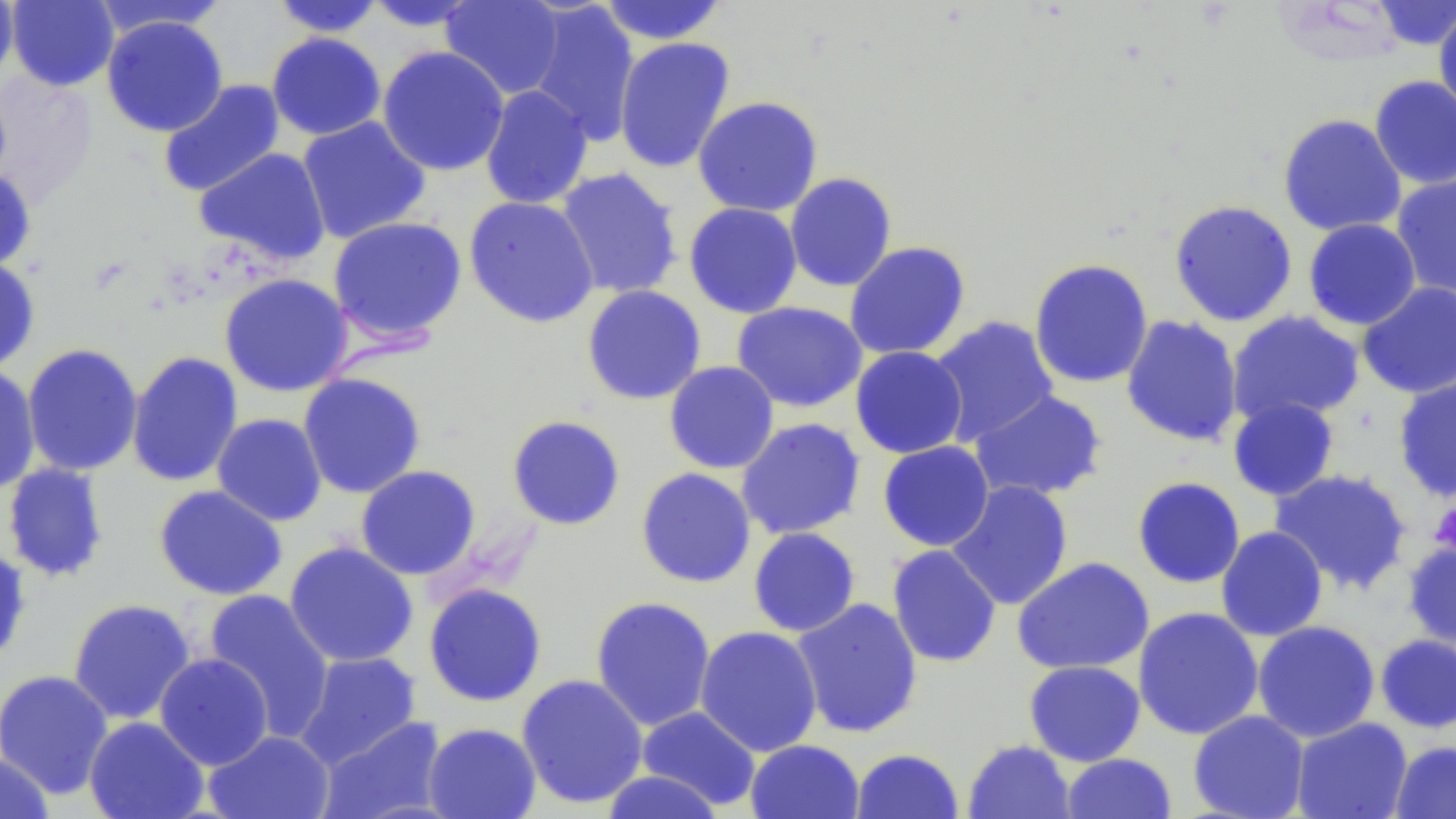
Summary:
  - Coordinate format: approximate bounding boxes as named x1/y1/x2/y2 corners in pixels
  - Platelet locations: (x1=1428, y1=501, x2=1456, y2=556)
  - Uninfected red blood cell locations: (x1=0, y1=0, x2=18, y2=87), (x1=6, y1=0, x2=120, y2=91), (x1=270, y1=0, x2=386, y2=37), (x1=440, y1=0, x2=566, y2=100), (x1=597, y1=0, x2=728, y2=45), (x1=361, y1=1, x2=485, y2=32), (x1=525, y1=1, x2=640, y2=145), (x1=1370, y1=1, x2=1456, y2=50), (x1=90, y1=2, x2=231, y2=39), (x1=1433, y1=8, x2=1456, y2=122), (x1=101, y1=15, x2=228, y2=137), (x1=266, y1=32, x2=386, y2=141), (x1=614, y1=37, x2=735, y2=173), (x1=377, y1=46, x2=509, y2=176), (x1=0, y1=73, x2=98, y2=204), (x1=1369, y1=75, x2=1456, y2=189), (x1=157, y1=79, x2=285, y2=198), (x1=480, y1=85, x2=594, y2=210), (x1=692, y1=96, x2=824, y2=217), (x1=1277, y1=113, x2=1407, y2=237), (x1=297, y1=116, x2=431, y2=244), (x1=194, y1=147, x2=331, y2=265), (x1=554, y1=167, x2=683, y2=299), (x1=0, y1=168, x2=36, y2=271), (x1=784, y1=172, x2=898, y2=292), (x1=1391, y1=173, x2=1456, y2=300), (x1=463, y1=196, x2=599, y2=329), (x1=1168, y1=199, x2=1298, y2=327), (x1=683, y1=202, x2=803, y2=318), (x1=327, y1=215, x2=467, y2=346), (x1=1303, y1=219, x2=1421, y2=330), (x1=844, y1=241, x2=971, y2=360), (x1=0, y1=258, x2=40, y2=372), (x1=1028, y1=258, x2=1154, y2=389), (x1=218, y1=273, x2=353, y2=397), (x1=1356, y1=281, x2=1456, y2=399), (x1=581, y1=285, x2=707, y2=405), (x1=731, y1=301, x2=867, y2=413), (x1=1226, y1=310, x2=1365, y2=426), (x1=1120, y1=314, x2=1243, y2=447), (x1=928, y1=315, x2=1060, y2=446), (x1=22, y1=343, x2=143, y2=477), (x1=850, y1=346, x2=968, y2=459), (x1=126, y1=351, x2=244, y2=488), (x1=664, y1=360, x2=780, y2=474), (x1=0, y1=365, x2=41, y2=496), (x1=298, y1=373, x2=426, y2=498), (x1=1393, y1=374, x2=1456, y2=501), (x1=970, y1=390, x2=1107, y2=502), (x1=1227, y1=397, x2=1340, y2=501), (x1=212, y1=413, x2=327, y2=526), (x1=506, y1=414, x2=626, y2=530), (x1=735, y1=417, x2=866, y2=540), (x1=877, y1=441, x2=994, y2=551), (x1=2, y1=463, x2=110, y2=583), (x1=355, y1=466, x2=481, y2=580), (x1=635, y1=467, x2=756, y2=588), (x1=1269, y1=468, x2=1412, y2=595), (x1=1132, y1=476, x2=1246, y2=589), (x1=947, y1=480, x2=1074, y2=610), (x1=153, y1=484, x2=287, y2=601), (x1=1215, y1=526, x2=1328, y2=641), (x1=748, y1=527, x2=861, y2=637), (x1=1403, y1=538, x2=1456, y2=655), (x1=283, y1=541, x2=419, y2=668), (x1=0, y1=543, x2=32, y2=666), (x1=886, y1=544, x2=1002, y2=668), (x1=1013, y1=557, x2=1154, y2=675), (x1=423, y1=583, x2=547, y2=707), (x1=201, y1=590, x2=336, y2=740), (x1=590, y1=595, x2=716, y2=731), (x1=791, y1=597, x2=923, y2=739), (x1=67, y1=598, x2=196, y2=725), (x1=1133, y1=606, x2=1264, y2=740), (x1=1252, y1=620, x2=1381, y2=743), (x1=695, y1=626, x2=823, y2=756), (x1=1375, y1=634, x2=1456, y2=734), (x1=295, y1=651, x2=421, y2=767), (x1=154, y1=653, x2=273, y2=770), (x1=1024, y1=660, x2=1146, y2=766), (x1=0, y1=669, x2=114, y2=799), (x1=516, y1=674, x2=648, y2=809), (x1=637, y1=706, x2=761, y2=810), (x1=1188, y1=710, x2=1310, y2=819), (x1=84, y1=716, x2=209, y2=819), (x1=318, y1=716, x2=448, y2=819), (x1=1290, y1=717, x2=1412, y2=819), (x1=423, y1=722, x2=541, y2=819), (x1=204, y1=730, x2=335, y2=819), (x1=745, y1=739, x2=865, y2=819), (x1=963, y1=740, x2=1076, y2=819), (x1=1389, y1=740, x2=1455, y2=818), (x1=851, y1=748, x2=964, y2=819), (x1=0, y1=751, x2=53, y2=819), (x1=1060, y1=752, x2=1177, y2=818), (x1=599, y1=769, x2=726, y2=819)
  - Slide-level diagnosis: negative for blood parasites
  - Stain: May-Grünwald-Giemsa
  - Preparation: thin blood smear
  - Field of view: single
  - Modality: light microscopy
  - Magnification: 1000x
  - Image size: 1456×819 pixels